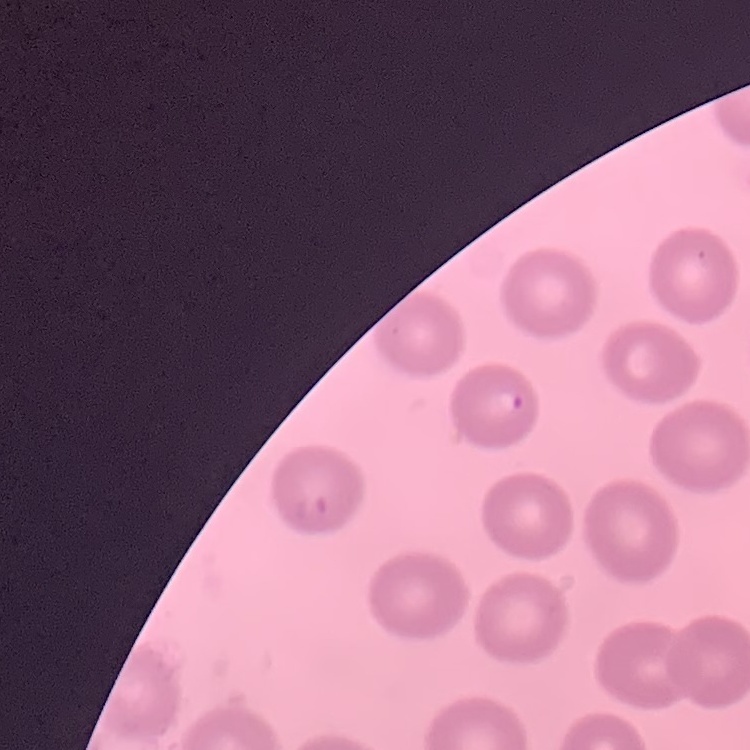

The red blood cells show no rouleaux formation. Stained with either Field's or Giemsa. Thin blood film. One tile cut from a larger photomicrograph.